Describe the morphology of the red blood cells.
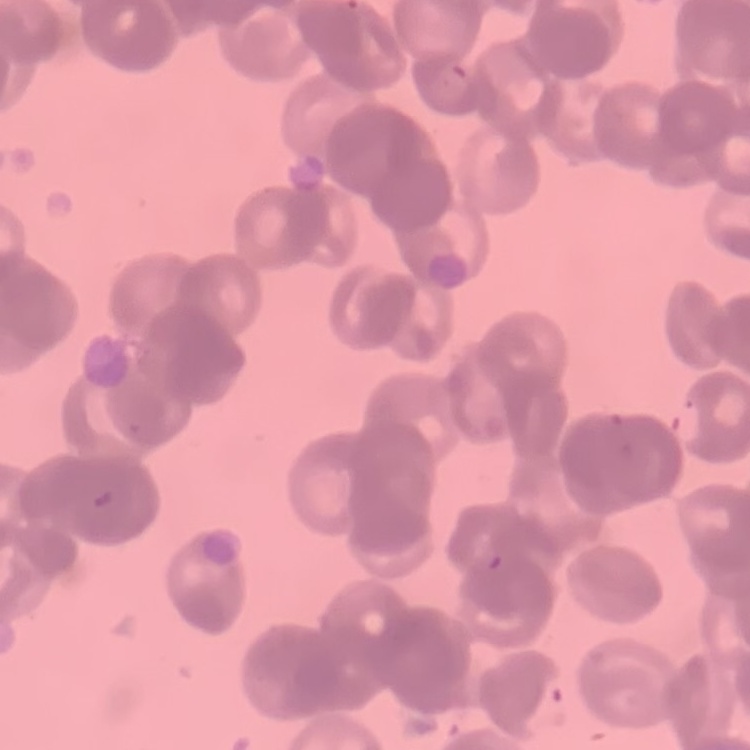

Rouleaux formation.

Square crop of a larger photomicrograph. Thin peripheral smear. Field's or Giemsa stain.